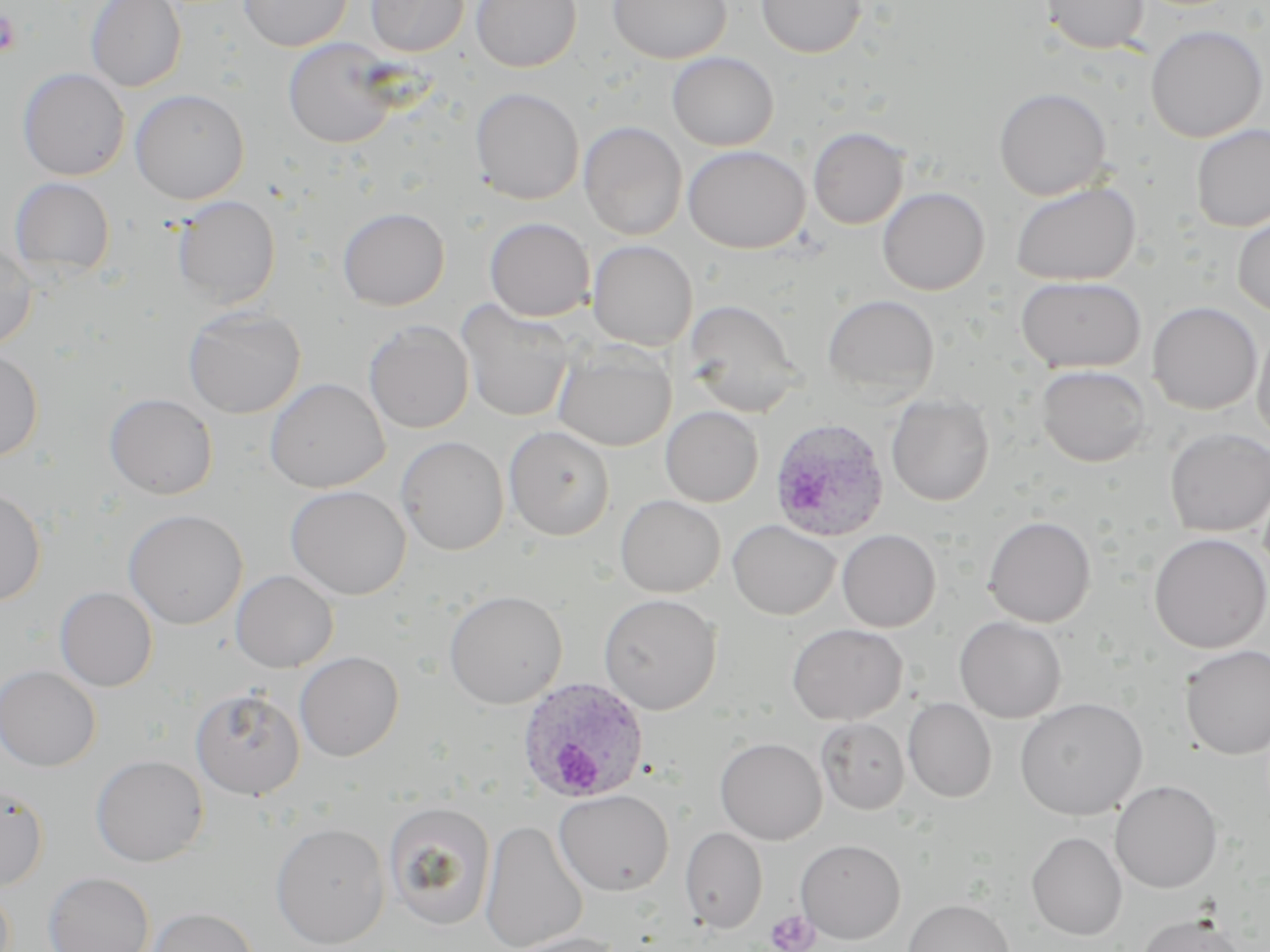
{
  "slide_level_diagnosis": "Plasmodium ovale",
  "uninfected_red_blood_cell_locations": "approximate bounding boxes as (x1, y1, x2, y2) in pixels: (86, 0, 186, 92), (239, 0, 352, 51), (366, 0, 469, 57), (471, 0, 582, 72), (608, 0, 731, 64), (756, 0, 866, 58), (1041, 0, 1149, 54), (1145, 25, 1268, 142), (283, 38, 400, 148), (667, 52, 779, 151), (18, 68, 130, 181), (470, 87, 584, 205), (994, 87, 1112, 201), (130, 89, 249, 204), (579, 121, 687, 240), (1191, 124, 1270, 231), (808, 127, 909, 229), (683, 145, 809, 253), (10, 177, 115, 278), (1010, 181, 1141, 286), (877, 186, 990, 295), (171, 195, 281, 308), (337, 207, 450, 310), (1232, 214, 1270, 319), (485, 217, 595, 321), (588, 240, 698, 351), (0, 243, 38, 351), (1015, 275, 1147, 373), (822, 294, 940, 399), (683, 299, 799, 415), (456, 300, 575, 422), (1147, 301, 1262, 414), (183, 306, 306, 418), (364, 321, 474, 434), (1252, 324, 1270, 447), (552, 344, 676, 451), (0, 348, 43, 463), (1036, 365, 1152, 467), (264, 377, 390, 493), (104, 393, 218, 499), (886, 394, 995, 506), (661, 406, 763, 507), (504, 425, 615, 540), (1165, 427, 1270, 536), (396, 436, 509, 556), (285, 484, 411, 600), (0, 485, 47, 606), (615, 494, 725, 597), (609, 505, 837, 602), (123, 509, 248, 628), (983, 515, 1096, 627), (728, 519, 840, 620), (837, 529, 941, 632), (1148, 533, 1270, 653), (231, 570, 338, 672), (55, 586, 158, 691), (443, 589, 567, 708), (598, 593, 722, 714), (954, 616, 1067, 722), (787, 623, 907, 725), (1180, 645, 1270, 761), (294, 651, 404, 761), (0, 664, 101, 771), (190, 686, 305, 800), (1015, 697, 1148, 821), (903, 698, 997, 802), (816, 718, 909, 815), (715, 737, 827, 844), (91, 754, 209, 867), (1110, 780, 1223, 893), (0, 784, 49, 891), (554, 789, 674, 895), (383, 801, 496, 930), (480, 819, 588, 952), (270, 822, 390, 948), (680, 827, 767, 933), (1026, 831, 1127, 940), (795, 839, 906, 943), (43, 871, 155, 952), (903, 898, 1015, 952), (143, 906, 258, 952), (1135, 913, 1247, 952), (500, 931, 625, 952)",
  "image_size": "1270×952 pixels",
  "stain": "May-Grünwald-Giemsa",
  "modality": "optical microscopy",
  "preparation": "thin blood film",
  "platelet_locations": "approximate bounding boxes as (x1, y1, x2, y2) in pixels: (0, 10, 22, 58), (765, 909, 818, 952)",
  "field_of_view": "one of a larger specimen",
  "magnification": "1000x",
  "plasmodium_ovale_infected_red_blood_cell_locations": "approximate bounding boxes as (x1, y1, x2, y2) in pixels: (768, 418, 891, 542), (516, 677, 650, 805)"
}